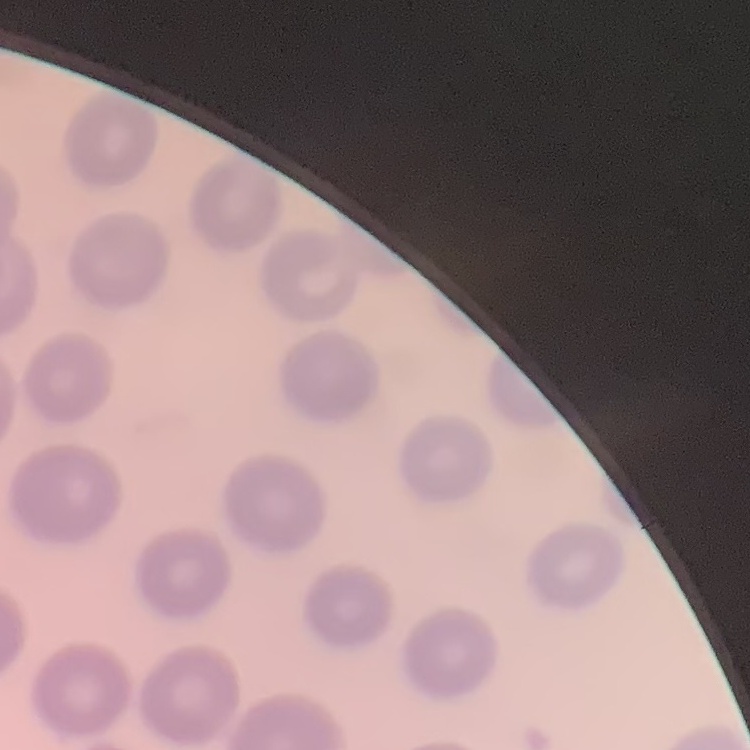
{
  "erythrocyte_morphology": "no rouleaux formation",
  "preparation": "thin blood smear",
  "image_type": "one tile cut from a larger photomicrograph",
  "stain": "Field's or Giemsa"
}